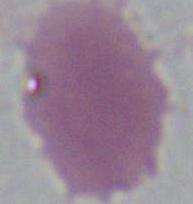
modality: micrograph
magnification: 1000x
identification: erythrocyte